Report the malaria status of this cell.
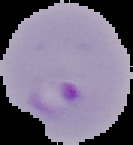

Parasitized.

Summary:
  - Image size: 133×145 pixels
  - Preparation: thin blood smear
  - Image type: segmented cell region on a black background